State the blood parasite species.
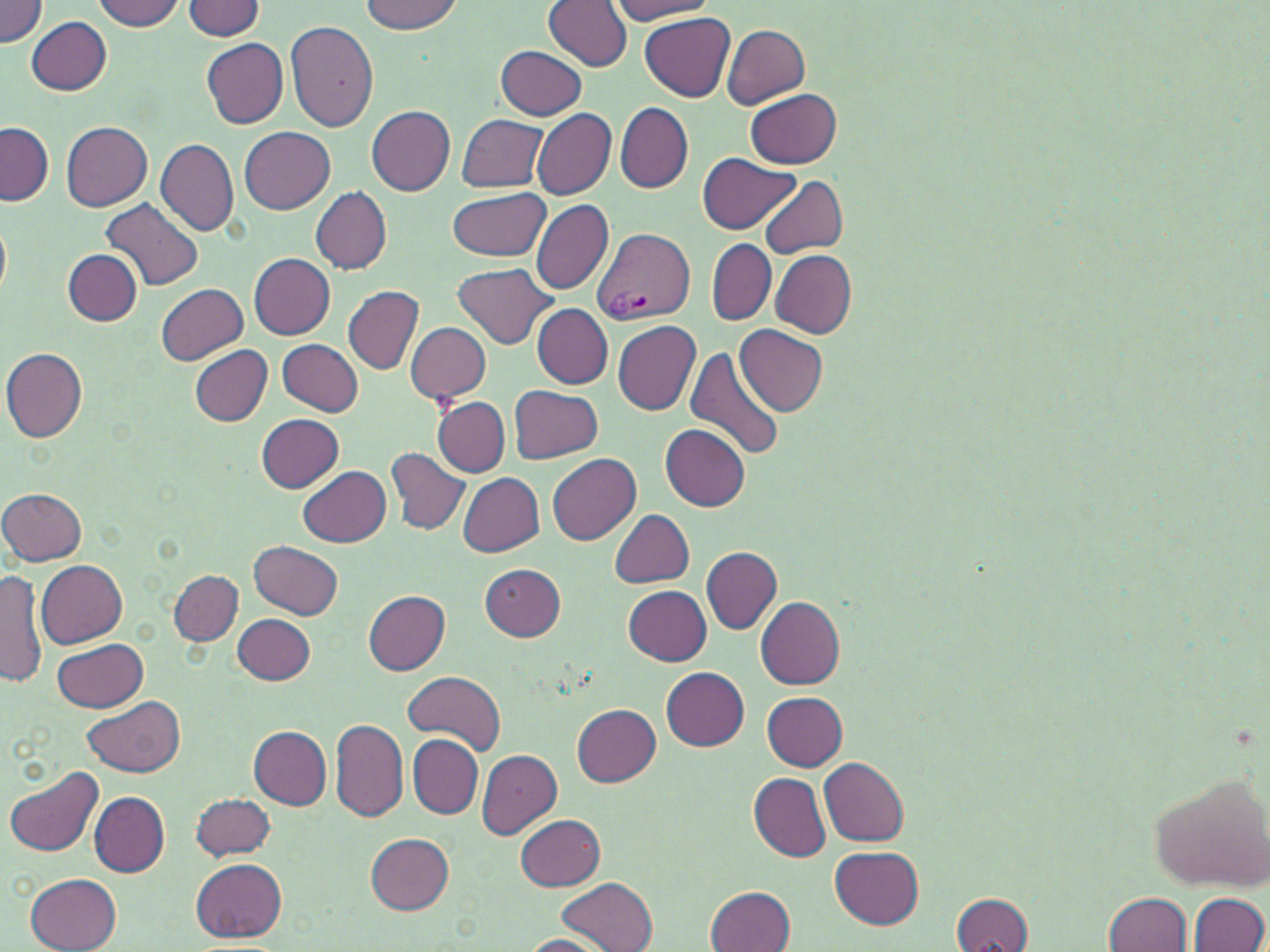

Plasmodium vivax.

Approximate bounding boxes as named x1/y1/x2/y2 corners in pixels. Uninfected red blood cell locations: (x1=0, y1=0, x2=47, y2=45), (x1=93, y1=0, x2=185, y2=31), (x1=360, y1=0, x2=463, y2=34), (x1=182, y1=1, x2=265, y2=38), (x1=544, y1=1, x2=632, y2=70), (x1=609, y1=1, x2=718, y2=23), (x1=641, y1=13, x2=735, y2=101), (x1=26, y1=15, x2=112, y2=95), (x1=286, y1=20, x2=378, y2=131), (x1=721, y1=24, x2=809, y2=107), (x1=201, y1=38, x2=287, y2=129), (x1=496, y1=45, x2=587, y2=121), (x1=746, y1=89, x2=843, y2=168), (x1=616, y1=103, x2=693, y2=192), (x1=366, y1=106, x2=455, y2=195), (x1=533, y1=107, x2=616, y2=200), (x1=456, y1=114, x2=548, y2=193), (x1=0, y1=122, x2=54, y2=206), (x1=61, y1=122, x2=151, y2=210), (x1=240, y1=126, x2=335, y2=214), (x1=155, y1=136, x2=238, y2=236), (x1=698, y1=153, x2=800, y2=234), (x1=758, y1=176, x2=848, y2=258), (x1=311, y1=187, x2=392, y2=274), (x1=445, y1=190, x2=551, y2=260), (x1=101, y1=198, x2=202, y2=291), (x1=531, y1=199, x2=613, y2=295), (x1=0, y1=217, x2=11, y2=296), (x1=707, y1=239, x2=774, y2=324), (x1=63, y1=249, x2=143, y2=326), (x1=771, y1=249, x2=857, y2=339), (x1=249, y1=252, x2=334, y2=339), (x1=454, y1=262, x2=556, y2=349), (x1=156, y1=283, x2=247, y2=366), (x1=343, y1=284, x2=424, y2=374), (x1=533, y1=304, x2=612, y2=388), (x1=612, y1=319, x2=701, y2=417), (x1=405, y1=321, x2=491, y2=403), (x1=736, y1=326, x2=827, y2=415), (x1=279, y1=339, x2=364, y2=415), (x1=686, y1=345, x2=784, y2=463), (x1=1, y1=346, x2=87, y2=442), (x1=189, y1=346, x2=271, y2=425), (x1=510, y1=385, x2=603, y2=463), (x1=421, y1=393, x2=513, y2=548), (x1=433, y1=396, x2=510, y2=477), (x1=255, y1=414, x2=344, y2=492), (x1=660, y1=424, x2=750, y2=511), (x1=387, y1=449, x2=469, y2=534), (x1=548, y1=453, x2=640, y2=546), (x1=298, y1=465, x2=390, y2=547), (x1=458, y1=472, x2=544, y2=558), (x1=0, y1=487, x2=87, y2=566), (x1=610, y1=509, x2=693, y2=587), (x1=249, y1=540, x2=342, y2=619), (x1=700, y1=547, x2=781, y2=634), (x1=38, y1=561, x2=128, y2=648), (x1=480, y1=564, x2=566, y2=642), (x1=0, y1=568, x2=46, y2=692), (x1=169, y1=570, x2=242, y2=646), (x1=623, y1=585, x2=712, y2=665), (x1=363, y1=589, x2=450, y2=674), (x1=756, y1=597, x2=845, y2=689), (x1=234, y1=613, x2=314, y2=685), (x1=53, y1=638, x2=147, y2=711), (x1=662, y1=667, x2=749, y2=750), (x1=403, y1=671, x2=505, y2=749), (x1=762, y1=692, x2=848, y2=770), (x1=82, y1=697, x2=186, y2=776), (x1=571, y1=703, x2=660, y2=785), (x1=331, y1=720, x2=410, y2=821), (x1=249, y1=726, x2=332, y2=808), (x1=408, y1=736, x2=482, y2=818), (x1=477, y1=750, x2=561, y2=839), (x1=819, y1=758, x2=909, y2=845), (x1=6, y1=765, x2=104, y2=859), (x1=1149, y1=771, x2=1270, y2=892), (x1=748, y1=773, x2=831, y2=861), (x1=189, y1=792, x2=274, y2=861), (x1=91, y1=793, x2=169, y2=877), (x1=515, y1=813, x2=605, y2=891), (x1=365, y1=833, x2=453, y2=914), (x1=830, y1=845, x2=925, y2=927), (x1=191, y1=858, x2=287, y2=942), (x1=26, y1=873, x2=122, y2=952), (x1=557, y1=876, x2=658, y2=952), (x1=706, y1=884, x2=795, y2=952), (x1=949, y1=892, x2=1035, y2=952), (x1=1104, y1=893, x2=1193, y2=952), (x1=1188, y1=893, x2=1268, y2=951), (x1=520, y1=934, x2=611, y2=951). Plasmodium vivax-infected red blood cell locations: (x1=592, y1=227, x2=694, y2=327). May-Grünwald-Giemsa-stained preparation. Light microscopy. Image is 1270×952 pixels. One field of a larger specimen. Thin blood film. Captured at 1000x magnification.